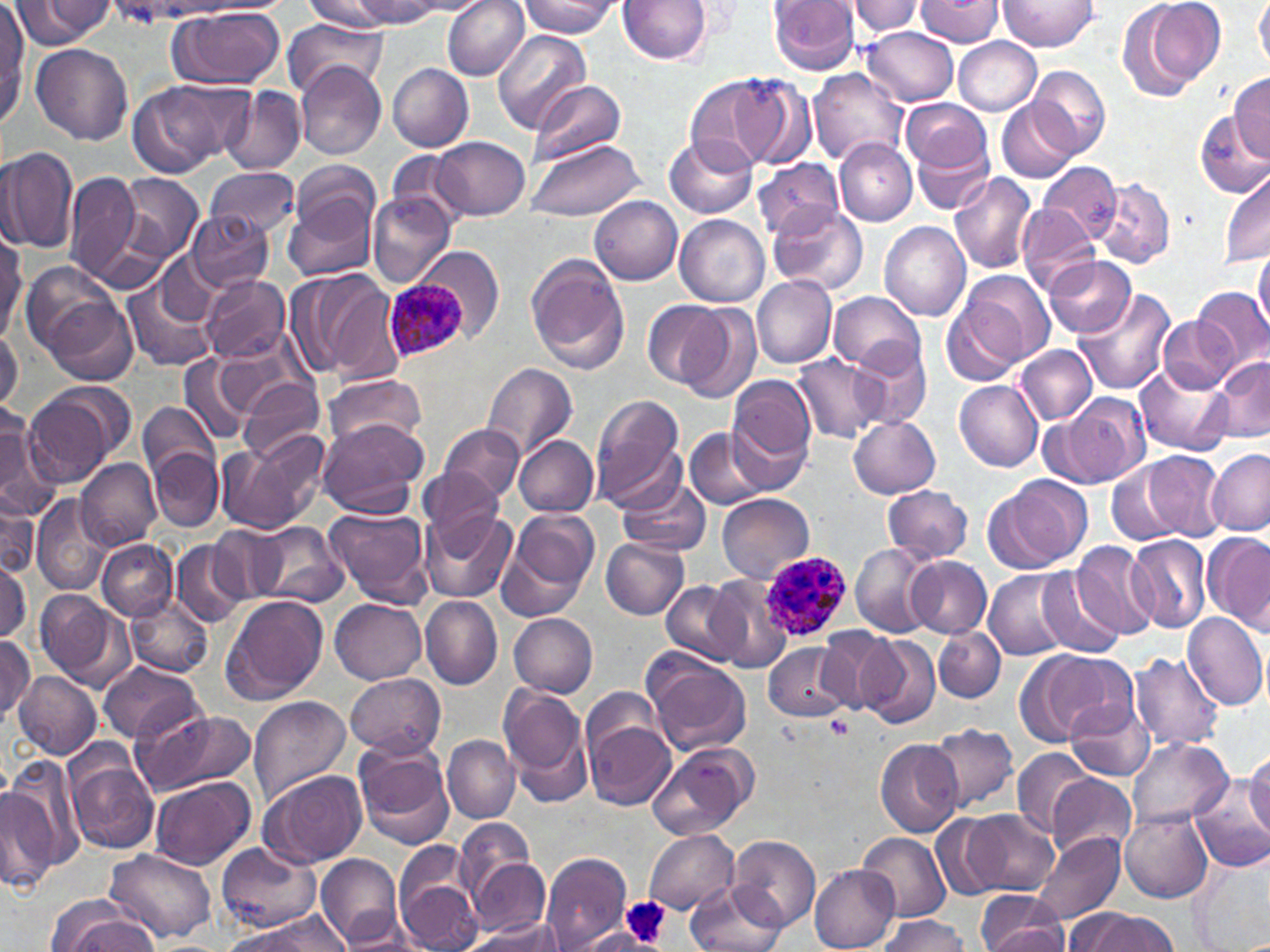

Summary:
  - Coordinate format: approximate bounding boxes as (x1, y1, x2, y2) in pixels
  - Platelet locations: (826, 715, 856, 741), (622, 896, 670, 950)
  - Plasmodium ovale-infected red blood cell locations: (385, 276, 469, 363), (759, 551, 851, 641)
  - Uninfected red blood cell locations: (9, 0, 113, 50), (442, 0, 530, 79), (519, 0, 619, 38), (619, 0, 714, 65), (769, 0, 861, 75), (848, 0, 923, 38), (913, 0, 1003, 46), (1000, 0, 1100, 52), (1116, 0, 1223, 101), (1255, 0, 1270, 72), (197, 1, 295, 15), (301, 1, 394, 32), (349, 1, 448, 27), (0, 7, 29, 128), (168, 7, 286, 89), (283, 17, 386, 100), (863, 27, 959, 106), (493, 30, 591, 133), (953, 38, 1041, 115), (31, 44, 134, 147), (296, 60, 386, 161), (388, 62, 474, 151), (1030, 65, 1111, 158), (809, 68, 909, 167), (728, 72, 817, 168), (1231, 73, 1270, 163), (686, 75, 776, 172), (129, 79, 232, 179), (527, 81, 626, 168), (221, 87, 305, 176), (997, 97, 1078, 182), (901, 98, 990, 174), (1194, 113, 1270, 200), (665, 134, 758, 218), (908, 134, 995, 214), (434, 137, 531, 220), (835, 138, 918, 227), (523, 139, 647, 221), (0, 144, 78, 254), (384, 150, 467, 226), (753, 157, 846, 242), (296, 158, 379, 234), (1037, 160, 1121, 242), (207, 167, 300, 240), (65, 170, 142, 285), (1220, 171, 1270, 264), (949, 172, 1038, 275), (116, 173, 202, 260), (1093, 176, 1176, 269), (281, 185, 380, 282), (367, 192, 454, 289), (591, 196, 683, 286), (769, 204, 869, 294), (1017, 205, 1097, 295), (187, 211, 274, 292), (675, 214, 769, 307), (879, 221, 970, 323), (0, 239, 25, 340), (417, 246, 504, 342), (1253, 247, 1270, 336), (155, 253, 222, 329), (525, 253, 630, 375), (1043, 256, 1137, 339), (22, 264, 124, 360), (291, 266, 395, 383), (960, 271, 1054, 367), (199, 274, 289, 363), (752, 276, 837, 369), (123, 282, 215, 372), (1191, 286, 1268, 372), (1073, 287, 1174, 395), (829, 292, 925, 372), (35, 295, 137, 388), (943, 298, 1027, 388), (644, 300, 729, 390), (678, 303, 762, 404), (1159, 315, 1236, 392), (0, 331, 22, 416), (850, 341, 932, 430), (1015, 346, 1096, 425), (179, 353, 252, 447), (792, 354, 887, 443), (1214, 355, 1270, 444), (1137, 361, 1233, 455), (482, 362, 579, 462), (727, 374, 817, 474), (322, 375, 429, 452), (237, 378, 323, 464), (953, 380, 1042, 470), (24, 384, 130, 487), (1050, 393, 1151, 488), (591, 395, 685, 506), (138, 403, 218, 483), (0, 404, 48, 513), (848, 414, 941, 498), (316, 417, 425, 518), (439, 422, 525, 507), (685, 430, 768, 510), (216, 434, 328, 537), (514, 435, 597, 516), (149, 447, 223, 530), (1207, 450, 1270, 536), (1141, 451, 1227, 542), (75, 456, 162, 552), (1107, 461, 1186, 546), (420, 467, 505, 546), (618, 477, 711, 559), (985, 477, 1090, 571), (883, 483, 974, 564), (0, 488, 39, 582), (30, 494, 112, 595), (717, 494, 814, 582), (324, 505, 434, 609), (418, 508, 516, 605), (503, 508, 599, 612), (252, 521, 349, 608), (211, 525, 286, 604), (1127, 532, 1212, 635), (1202, 533, 1269, 631), (97, 538, 177, 621), (601, 538, 689, 619), (172, 541, 248, 628), (1070, 542, 1159, 641), (852, 545, 936, 638), (905, 556, 991, 637), (0, 557, 31, 646), (1036, 568, 1124, 656), (986, 569, 1077, 658), (707, 575, 794, 674), (661, 580, 746, 666), (35, 590, 135, 692), (221, 594, 329, 704), (124, 596, 214, 680), (420, 597, 501, 689), (330, 598, 426, 683), (508, 611, 598, 699), (1182, 611, 1270, 710), (935, 626, 1005, 703), (818, 628, 906, 713), (855, 633, 940, 730), (0, 634, 35, 720), (763, 642, 856, 722), (1031, 650, 1135, 740), (1127, 652, 1226, 752), (646, 658, 753, 756), (98, 661, 205, 745), (15, 671, 100, 761), (346, 673, 445, 758), (500, 684, 593, 799), (248, 696, 350, 805), (1064, 698, 1154, 781), (132, 707, 255, 796), (584, 717, 675, 811), (929, 724, 1018, 814), (442, 737, 520, 823), (1127, 737, 1232, 828), (874, 739, 963, 838), (354, 740, 454, 848), (650, 742, 759, 838), (1012, 748, 1095, 837), (1246, 750, 1270, 840), (64, 752, 159, 855), (7, 756, 82, 870), (256, 770, 365, 869), (1048, 774, 1135, 862), (148, 777, 255, 870), (1191, 780, 1270, 874), (0, 781, 57, 894), (1118, 808, 1212, 902), (965, 810, 1056, 895), (933, 815, 1010, 901), (453, 819, 537, 912), (645, 830, 737, 913), (855, 831, 950, 924), (1030, 832, 1123, 925), (728, 834, 820, 934), (217, 843, 319, 933), (104, 848, 217, 945), (315, 852, 401, 947), (542, 853, 631, 950), (471, 856, 550, 937), (1188, 858, 1268, 952), (811, 866, 898, 952), (396, 867, 482, 952), (686, 882, 787, 952), (976, 891, 1068, 952), (55, 909, 158, 952), (338, 910, 431, 952), (1068, 910, 1177, 952), (229, 914, 350, 950), (880, 915, 971, 952), (471, 918, 561, 950), (574, 928, 647, 951)
  - Slide-level diagnosis: Plasmodium ovale
  - Preparation: thin blood film
  - Field of view: one of a larger specimen
  - Modality: light microscopy
  - Magnification: 1000x
  - Stain: May-Grünwald-Giemsa
  - Image size: 1270×952 pixels